Classify this cell by malaria status.
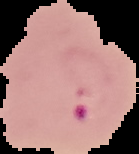
It is parasitized.

Summary:
  - Preparation: thin blood smear
  - Image type: segmented cell region with the area outside set to black
  - Image size: 139×154 pixels